Identify the cell.
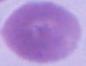

This is an erythrocyte.

{
  "modality": "micrograph",
  "magnification": "1000x"
}